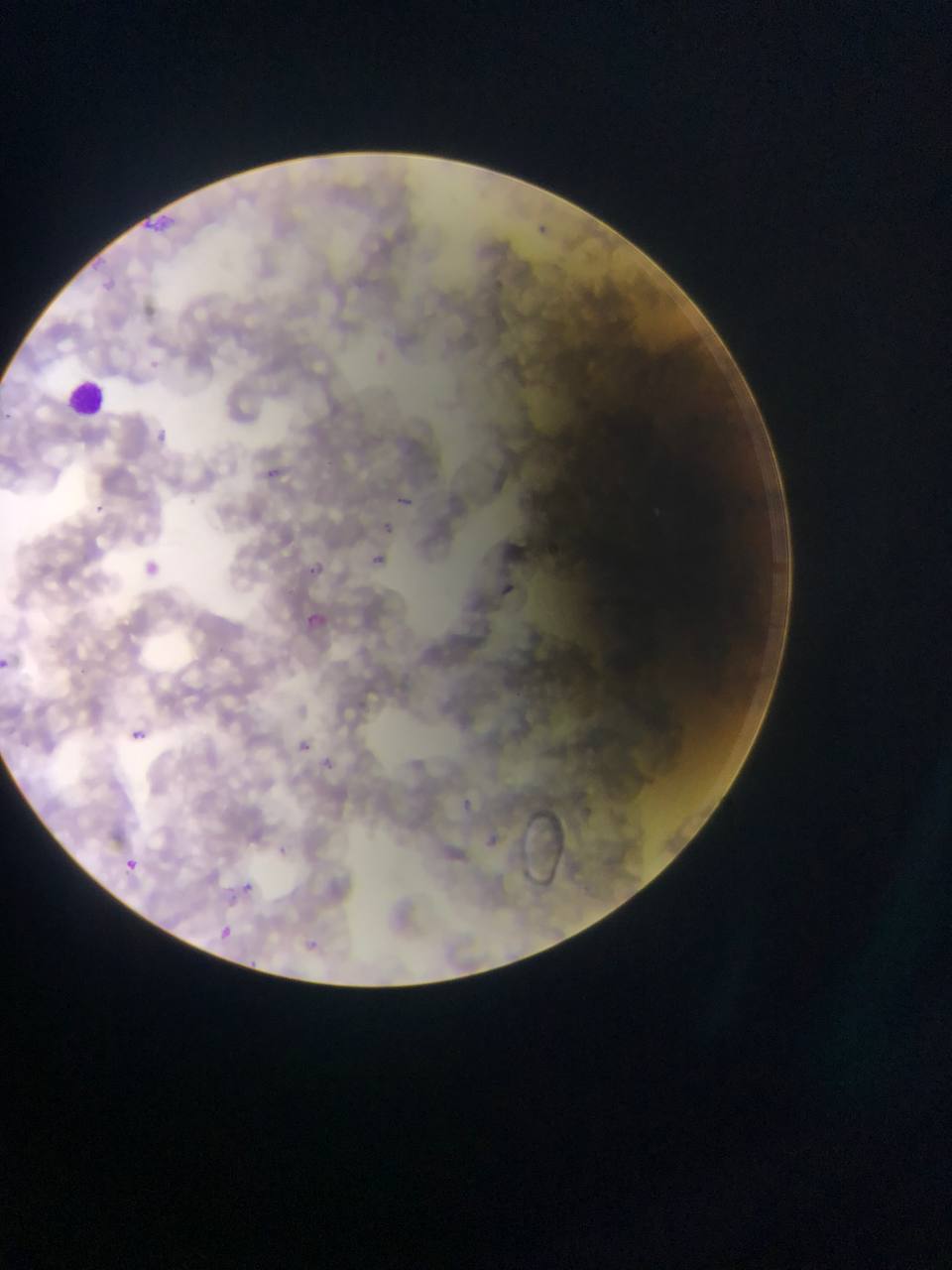
Approximate bounding boxes as [left, top, right, bottom] in pixels. Leukocyte locations: [59, 376, 109, 422]. Malaria parasite locations: [262, 464, 292, 486], [396, 493, 416, 506], [92, 500, 110, 517], [381, 523, 395, 533], [366, 552, 388, 572], [138, 558, 162, 580], [304, 562, 324, 581], [499, 578, 512, 597], [301, 609, 330, 637], [0, 657, 12, 670], [128, 728, 145, 743], [291, 736, 316, 759], [326, 758, 334, 774], [123, 858, 139, 873], [237, 880, 255, 897], [214, 924, 236, 945], [299, 933, 328, 957], [245, 957, 261, 973]. One field of view. Mobile-phone photograph taken through the microscope. Thin blood smear. Collected in Ghana. Image is 952×1270 pixels.